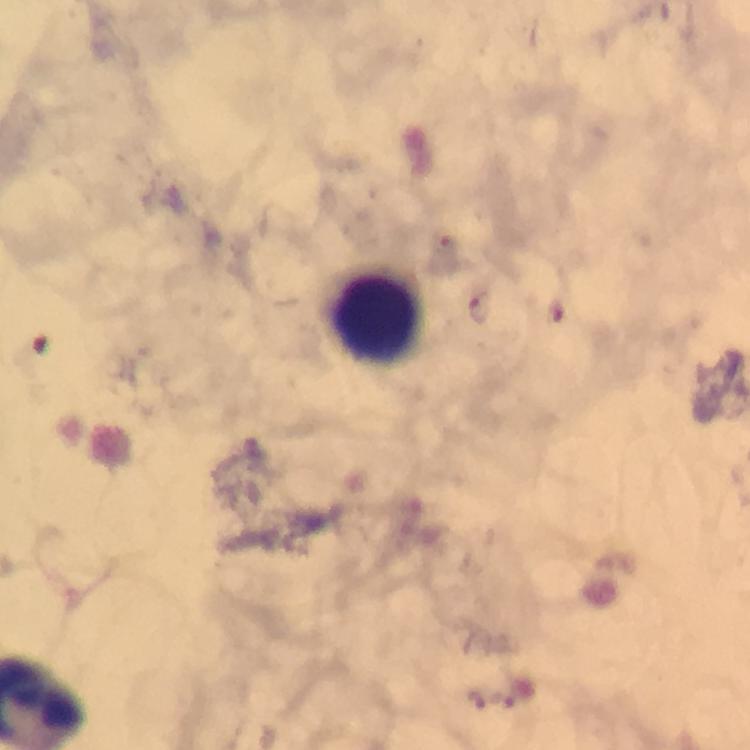
Approximate centers as {x, y} in pixels.
Summary:
  - Leukocyte locations: {378, 319}
  - Plasmodium parasite locations: {445, 246}, {482, 310}, {477, 699}, {503, 702}
  - Context: from a malaria diagnostic workup
  - Immersion oil: used
  - Magnification: 100x
  - Preparation: thick smear
  - Stain: Giemsa
  - Image size: 750×750 pixels
  - Capture: smartphone mounted on the microscope
  - Cropped from: one field of view